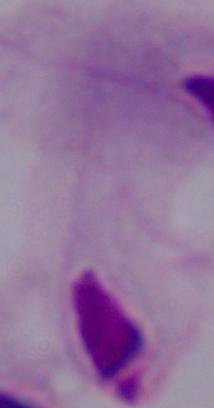

Summary:
  - Magnification: 1000x
  - Identification: trichomonad
  - Modality: micrograph